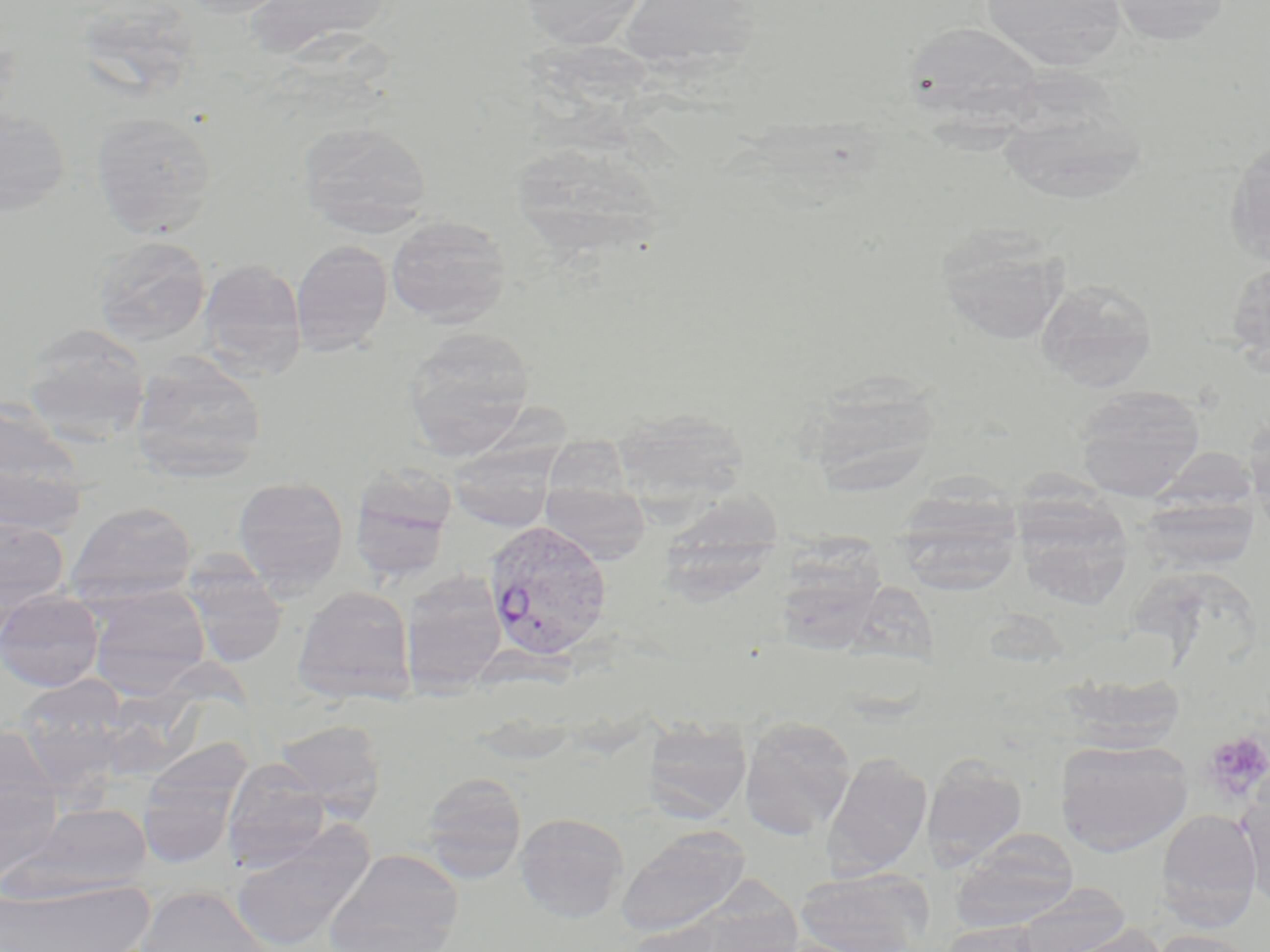

slide-level diagnosis = Plasmodium vivax
stain = May-Grünwald-Giemsa
magnification = 1000x
modality = light microscopy
platelet locations = approximate bounding boxes as [x1, y1, x2, y2] in pixels: [1203, 732, 1270, 802]
uninfected red blood cell locations = approximate bounding boxes as [x1, y1, x2, y2] in pixels: [177, 0, 294, 18], [244, 0, 396, 62], [516, 0, 649, 49], [617, 0, 763, 73], [980, 0, 1128, 70], [1109, 0, 1231, 47], [902, 20, 1045, 124], [995, 84, 1148, 205], [0, 106, 72, 216], [90, 110, 218, 238], [298, 119, 433, 237], [1223, 139, 1270, 266], [510, 140, 667, 259], [385, 215, 511, 327], [936, 225, 1070, 345], [92, 234, 212, 346], [290, 240, 392, 355], [196, 259, 307, 379], [1226, 260, 1270, 373], [1036, 279, 1157, 392], [20, 322, 151, 441], [402, 326, 536, 458], [129, 353, 267, 482], [800, 375, 941, 496], [1072, 385, 1206, 501], [0, 398, 87, 519], [466, 399, 580, 537], [611, 407, 749, 516], [1243, 412, 1270, 523], [543, 441, 632, 505], [0, 455, 87, 540], [348, 468, 457, 583], [232, 477, 349, 597], [541, 482, 652, 563], [661, 484, 782, 620], [894, 487, 1024, 595], [1012, 492, 1135, 609], [1138, 497, 1259, 573], [65, 500, 199, 603], [0, 515, 69, 614], [787, 528, 887, 660], [180, 557, 288, 667], [400, 571, 507, 693], [85, 585, 211, 695], [292, 585, 416, 703], [0, 589, 105, 691], [1059, 672, 1186, 751], [14, 676, 130, 784], [739, 715, 857, 840], [642, 717, 751, 823], [273, 718, 387, 819], [0, 726, 60, 823], [1056, 738, 1192, 856], [137, 750, 247, 868], [821, 752, 932, 879], [922, 755, 1028, 869], [222, 760, 331, 869], [418, 771, 528, 880], [1237, 772, 1270, 905], [0, 782, 64, 887], [16, 802, 152, 898], [1155, 809, 1261, 928], [515, 812, 630, 922], [230, 823, 375, 952], [616, 827, 750, 937], [952, 828, 1080, 932], [324, 848, 464, 952], [794, 868, 934, 952], [0, 878, 152, 952], [1010, 883, 1132, 952], [135, 885, 271, 952], [616, 920, 733, 952], [940, 921, 1046, 952], [1051, 923, 1169, 952], [1150, 928, 1261, 952]
image size = 1270×952 pixels
Plasmodium vivax-infected red blood cell locations = approximate bounding boxes as [x1, y1, x2, y2] in pixels: [484, 519, 613, 661]
preparation = thin blood smear
field of view = one of a larger specimen